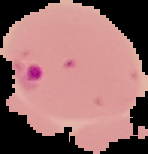
Image is 148×154 pixels. Segmented cell region on a black background. From a thin blood film. Malaria status: parasitized.